Locate and identify every blood parasite.
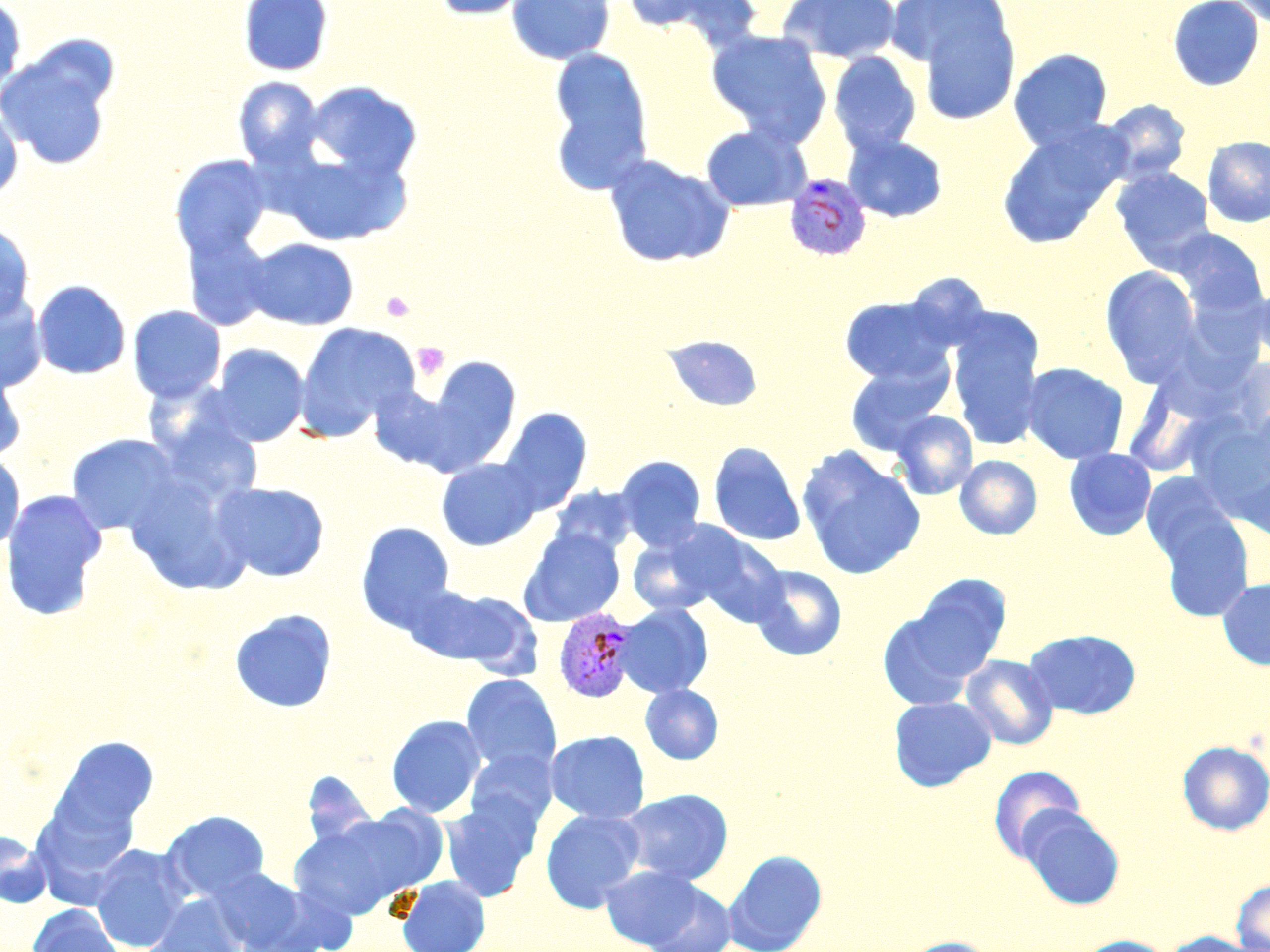

Approximate bounding boxes as (x1,y1)-(x2,y2) corner pairs in pixels.
Plasmodium vivax-infected red blood cells: (784,173)-(872,261), (554,608)-(638,702).
No Plasmodium falciparum, Plasmodium ovale, Plasmodium malariae, Babesia divergens, or Trypanosoma brucei observed.

Uninfected red blood cell locations: (238,0)-(333,77), (430,0)-(533,20), (506,0)-(615,64), (624,0)-(764,48), (777,0)-(902,64), (1167,0)-(1264,91), (0,1)-(27,99), (1229,1)-(1270,32), (907,2)-(1021,124), (706,30)-(832,146), (0,42)-(117,173), (548,48)-(654,193), (1009,48)-(1113,151), (829,52)-(922,156), (232,77)-(325,169), (305,81)-(422,180), (1100,99)-(1192,185), (0,106)-(24,202), (996,123)-(1129,249), (700,125)-(810,211), (843,134)-(948,223), (1202,136)-(1270,228), (273,148)-(412,247), (169,154)-(272,259), (603,154)-(735,269), (1111,167)-(1214,271), (0,222)-(35,325), (181,229)-(277,331), (1171,229)-(1267,318), (244,237)-(359,330), (1100,265)-(1201,386), (1251,276)-(1270,367), (32,280)-(131,380), (0,293)-(47,394), (839,295)-(955,385), (128,305)-(226,403), (947,310)-(1046,451), (296,322)-(420,438), (663,334)-(763,412), (210,344)-(310,447), (414,357)-(523,473), (844,358)-(953,456), (0,362)-(28,461), (1022,362)-(1128,464), (369,386)-(459,472), (498,409)-(592,515), (891,410)-(978,500), (67,434)-(183,536), (708,441)-(806,547), (798,449)-(925,579), (1064,449)-(1156,540), (0,452)-(24,554), (615,455)-(706,551), (955,455)-(1042,540), (436,458)-(542,551), (1142,472)-(1237,567), (211,481)-(329,583), (550,486)-(638,557), (0,489)-(108,621), (1156,508)-(1255,621), (355,523)-(456,635), (519,528)-(625,626), (627,530)-(724,617), (685,532)-(790,627), (748,564)-(847,661), (903,574)-(1011,684), (1217,577)-(1270,671), (412,585)-(541,675), (877,603)-(987,712), (615,604)-(713,698), (229,609)-(338,714), (1023,629)-(1140,719), (961,655)-(1059,750), (461,674)-(562,776), (640,685)-(723,764), (888,696)-(996,792), (386,714)-(486,818), (546,730)-(650,824), (51,735)-(159,840), (1178,740)-(1270,835), (465,748)-(558,833), (988,764)-(1086,863), (619,789)-(734,885), (439,797)-(540,902), (29,802)-(141,907), (327,806)-(451,903), (1019,807)-(1125,910), (540,809)-(645,912), (161,810)-(271,902), (289,820)-(420,919), (0,831)-(51,908), (89,844)-(193,952), (725,850)-(827,952), (600,865)-(704,949), (208,867)-(312,950), (397,875)-(490,952), (1230,878)-(1270,951), (642,880)-(738,952), (145,894)-(247,952), (27,904)-(124,952), (1161,931)-(1269,952), (899,936)-(999,952), (1072,936)-(1173,952). Platelet locations: (381,291)-(414,322), (412,342)-(450,380). Slide-level diagnosis: Plasmodium vivax. May-Grünwald-Giemsa-stained preparation. Image is 1270×952 pixels. Captured at 1000x magnification. Thin blood smear. One field of a larger specimen. Light microscopy.